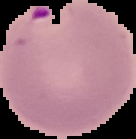 Image is 136×139 pixels. From a thin blood film. Segmented cell region on a black background. Result: malaria parasites detected.